Assess this cell for malaria.
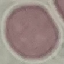
It is uninfected.

image type = automatically extracted cell patch, resized to 64 × 64 pixels
stain = Giemsa
capture = smartphone camera at the microscope eyepiece
preparation = thin smear